Classify this cell by malaria status.
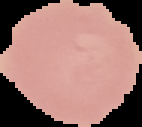
Uninfected.

The area outside the segmented cell region is set to black. From a thin blood film. Image is 142×127 pixels.